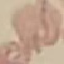

Malaria status: uninfected. Acquired by smartphone through the microscope eyepiece. Thin blood film. Cell patch, automatically extracted from a larger field of view and resized to 64 × 64 pixels. Giemsa-stained preparation.